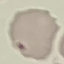
Result: no malaria parasites detected. Acquired by smartphone through the microscope eyepiece. Automatically extracted cell patch, resized to 64 × 64 pixels. Giemsa stain. Thin smear of blood.